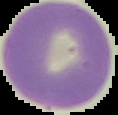
Summary:
  - Preparation: thin blood smear
  - Image type: cell region segmented out of the field of view; surrounding area masked to black
  - Malaria status: uninfected
  - Image size: 118×115 pixels